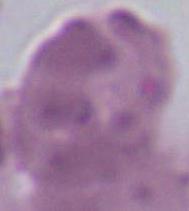
Summary:
  - Modality: micrograph
  - Identification: red blood cell
  - Magnification: 1000x